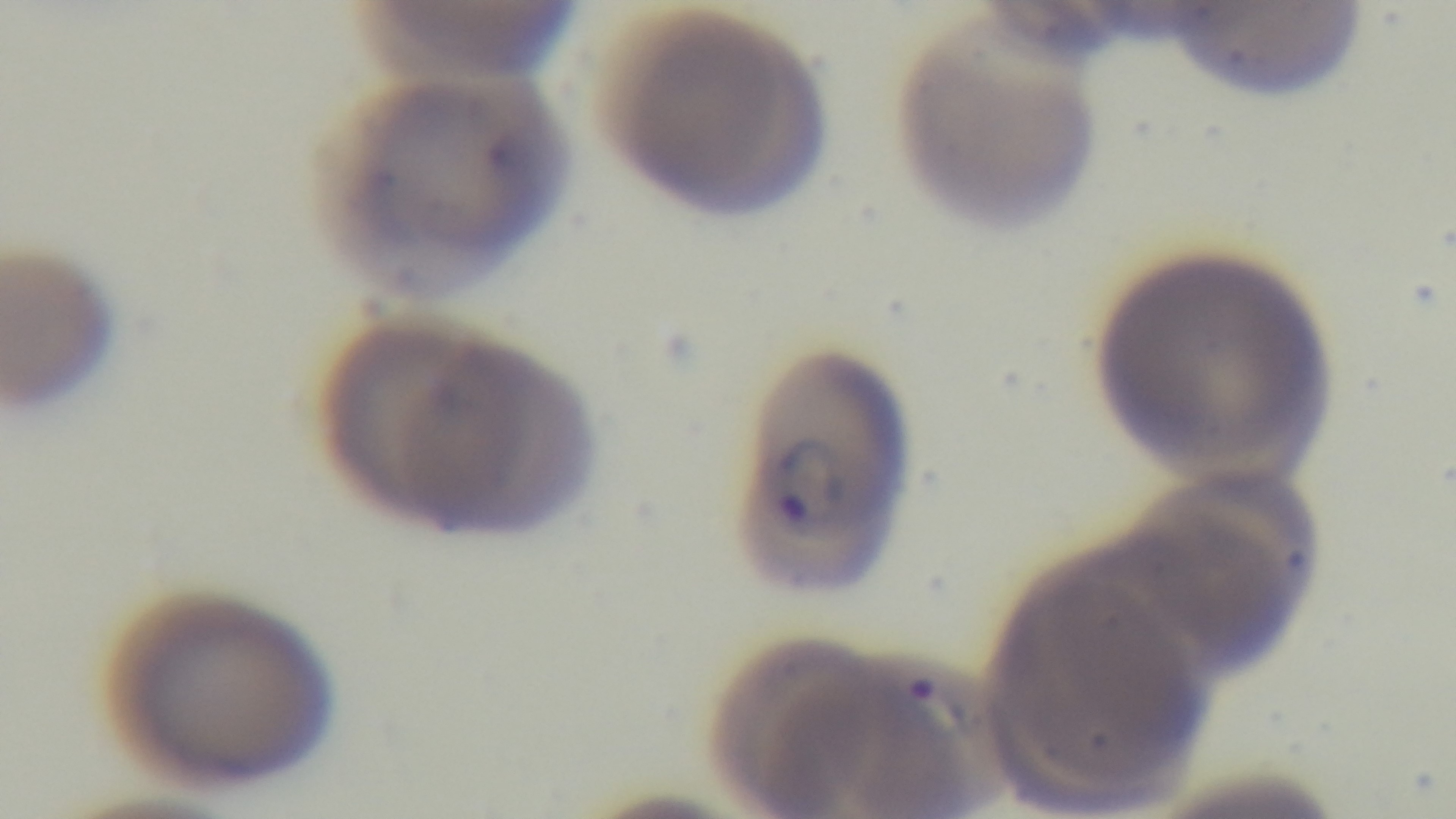 Light microscopy. Mounted 4K digital camera. Oil-immersion objective, 100x. Malaria status: positive. One field from the slide. Preparation: thin. Giemsa-stained.